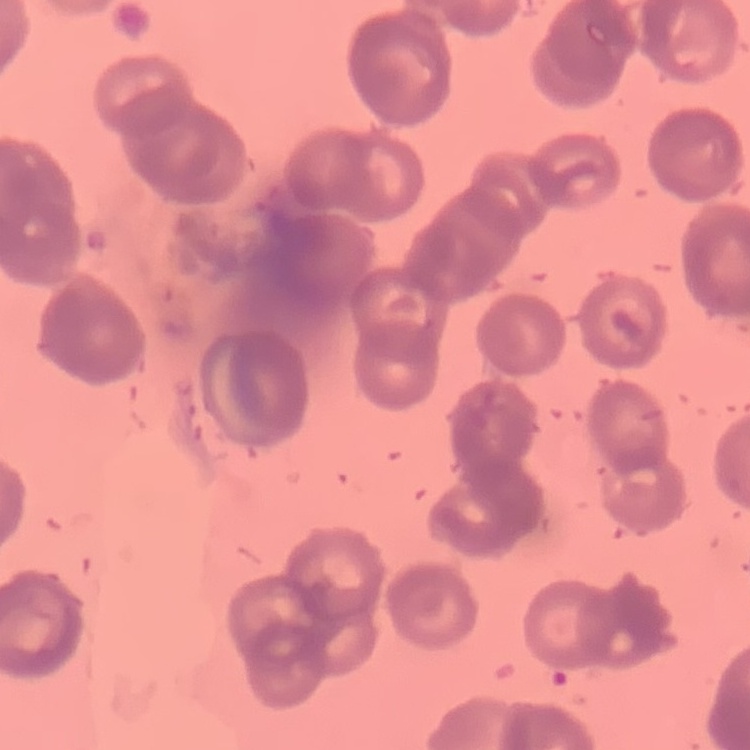

Summary:
  - Erythrocyte morphology: rouleaux formation
  - Image type: one tile cut from a larger photomicrograph
  - Preparation: thin peripheral smear
  - Stain: Field's or Giemsa